Locate platelets.
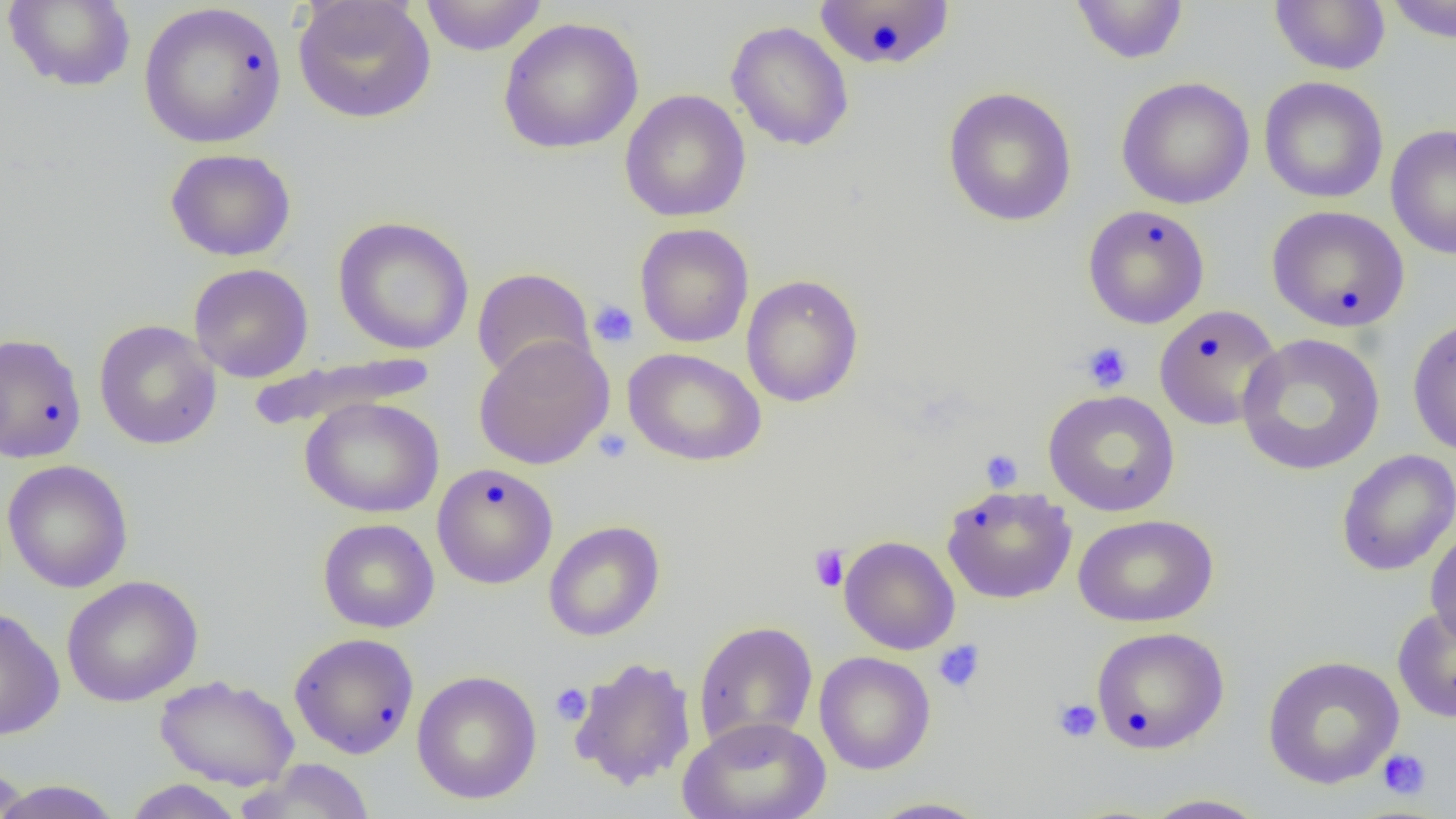
Approximate bounding boxes as (x1,y1)-(x2,y2) corner pairs in pixels.
Platelets: (588,300)-(639,348), (1081,341)-(1133,392), (593,428)-(633,464), (980,449)-(1023,492), (809,544)-(849,592), (934,639)-(986,692), (550,683)-(592,725), (1052,698)-(1102,742), (1378,748)-(1431,800).

slide-level diagnosis = negative for blood parasites
magnification = 1000x
uninfected red blood cell locations = approximate bounding boxes as (x1,y1)-(x2,y2) corner pairs in pixels: (292,0)-(436,124), (419,0)-(548,56), (813,0)-(956,72), (1269,0)-(1391,75), (1383,0)-(1456,43), (3,1)-(136,92), (1070,1)-(1190,65), (138,2)-(287,149), (497,16)-(644,155), (726,20)-(854,152), (1259,76)-(1389,204), (1115,77)-(1255,210), (942,86)-(1078,227), (620,89)-(751,222), (1386,124)-(1456,261), (165,148)-(297,262), (1083,204)-(1210,329), (1266,205)-(1410,332), (333,215)-(474,355), (634,223)-(754,347), (188,263)-(313,383), (471,267)-(595,384), (741,275)-(864,407), (1154,304)-(1282,431), (1407,316)-(1456,457), (94,319)-(222,450), (0,331)-(87,464), (1236,333)-(1385,476), (474,334)-(614,470), (623,347)-(766,467), (247,352)-(437,432), (1043,389)-(1181,516), (300,396)-(444,518), (1336,448)-(1456,577), (2,459)-(133,593), (432,463)-(558,589), (941,484)-(1077,604), (1073,513)-(1218,628), (318,518)-(440,633), (543,520)-(665,642), (1424,525)-(1456,649), (839,535)-(960,655), (61,575)-(202,706), (1392,605)-(1456,723), (0,607)-(65,741), (693,621)-(818,751), (1091,627)-(1229,753), (289,632)-(420,759), (814,651)-(936,775), (1262,655)-(1404,789), (569,656)-(697,790), (411,670)-(542,804), (155,675)-(299,790), (678,715)-(831,819), (0,760)-(31,819), (239,760)-(376,819), (123,779)-(246,818), (0,780)-(124,818), (1140,793)-(1272,818), (866,796)-(992,818)
image size = 1456×819 pixels
preparation = thin blood film
field of view = single
modality = light microscopy